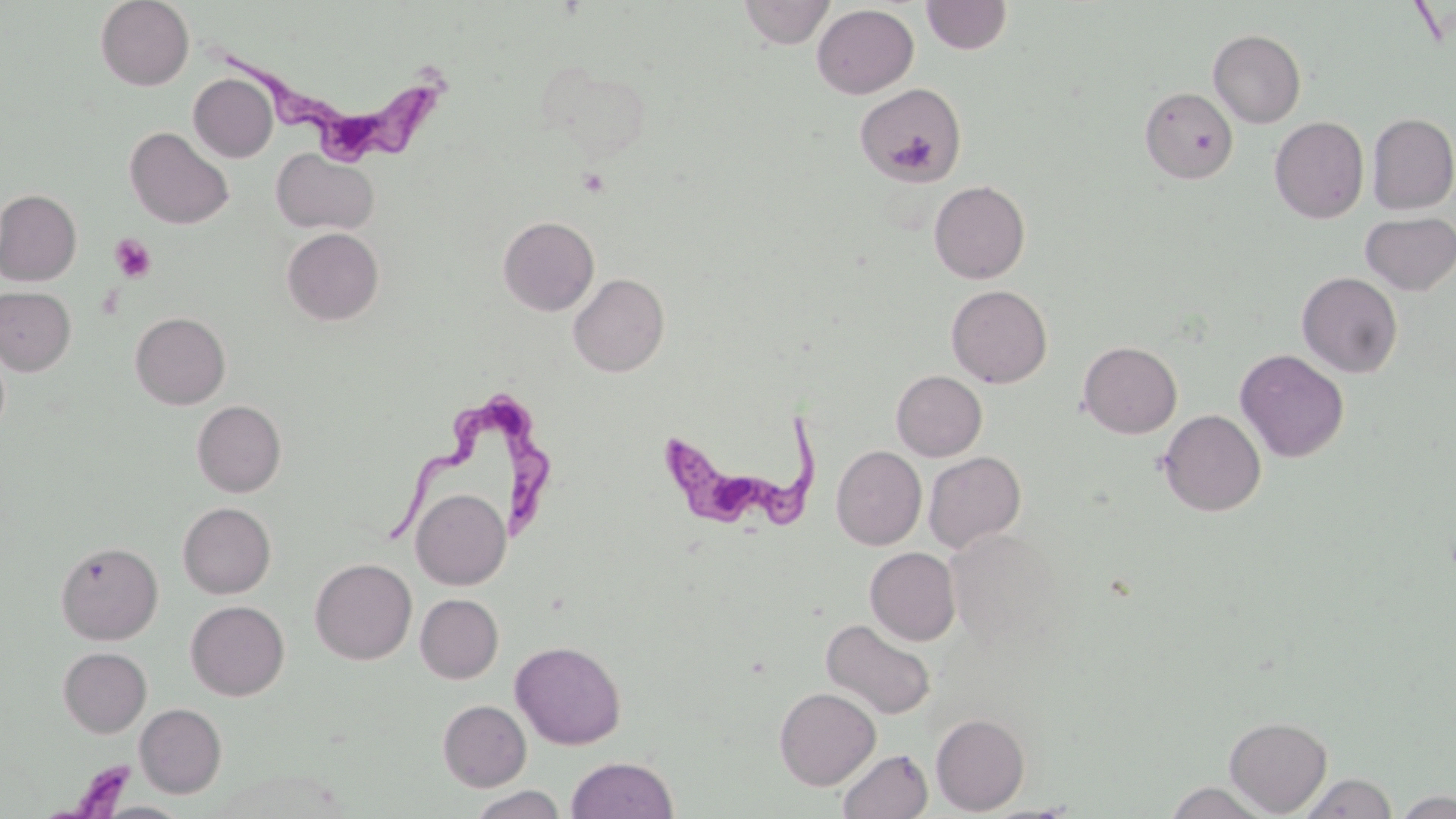

Summary:
  - Coordinate format: approximate bounding boxes as [x1, y1, x2, y2] in pixels
  - Platelet locations: [110, 234, 156, 282]
  - Uninfected red blood cell locations: [95, 0, 193, 90], [738, 0, 835, 48], [921, 0, 1012, 55], [812, 4, 918, 98], [1208, 29, 1305, 128], [539, 60, 655, 162], [189, 74, 277, 162], [854, 83, 967, 186], [1139, 87, 1238, 184], [1368, 112, 1456, 214], [1270, 117, 1369, 223], [125, 126, 234, 229], [272, 148, 378, 235], [929, 180, 1030, 284], [0, 189, 81, 286], [1359, 211, 1456, 296], [498, 216, 599, 315], [281, 227, 384, 326], [1297, 271, 1403, 378], [569, 273, 669, 377], [946, 285, 1052, 388], [0, 286, 76, 375], [130, 312, 230, 409], [1078, 341, 1182, 438], [1235, 349, 1349, 463], [892, 370, 987, 461], [193, 400, 286, 497], [1158, 409, 1266, 517], [831, 446, 926, 549], [923, 451, 1026, 552], [411, 488, 511, 590], [178, 502, 276, 598], [944, 528, 1061, 648], [55, 541, 163, 645], [865, 547, 960, 645], [310, 558, 417, 664], [415, 594, 503, 683], [185, 600, 289, 700], [820, 618, 936, 720], [510, 640, 626, 749], [58, 647, 151, 737], [774, 687, 880, 790], [438, 699, 531, 791], [135, 703, 226, 797], [931, 713, 1029, 815], [1224, 716, 1332, 816], [837, 747, 933, 819], [566, 756, 679, 819], [1298, 773, 1398, 818], [1164, 781, 1270, 818], [465, 786, 569, 818], [1393, 790, 1455, 817], [96, 802, 191, 819]
  - Trypanosoma brucei locations: [227, 43, 446, 164], [370, 392, 566, 548], [651, 423, 814, 535], [54, 753, 139, 818]
  - Slide-level diagnosis: Trypanosoma brucei
  - Modality: optical microscopy
  - Field of view: one of a larger specimen
  - Image size: 1456×819 pixels
  - Stain: May-Grünwald-Giemsa
  - Preparation: thin blood film
  - Magnification: 1000x